Give the position of every leukocyte visible.
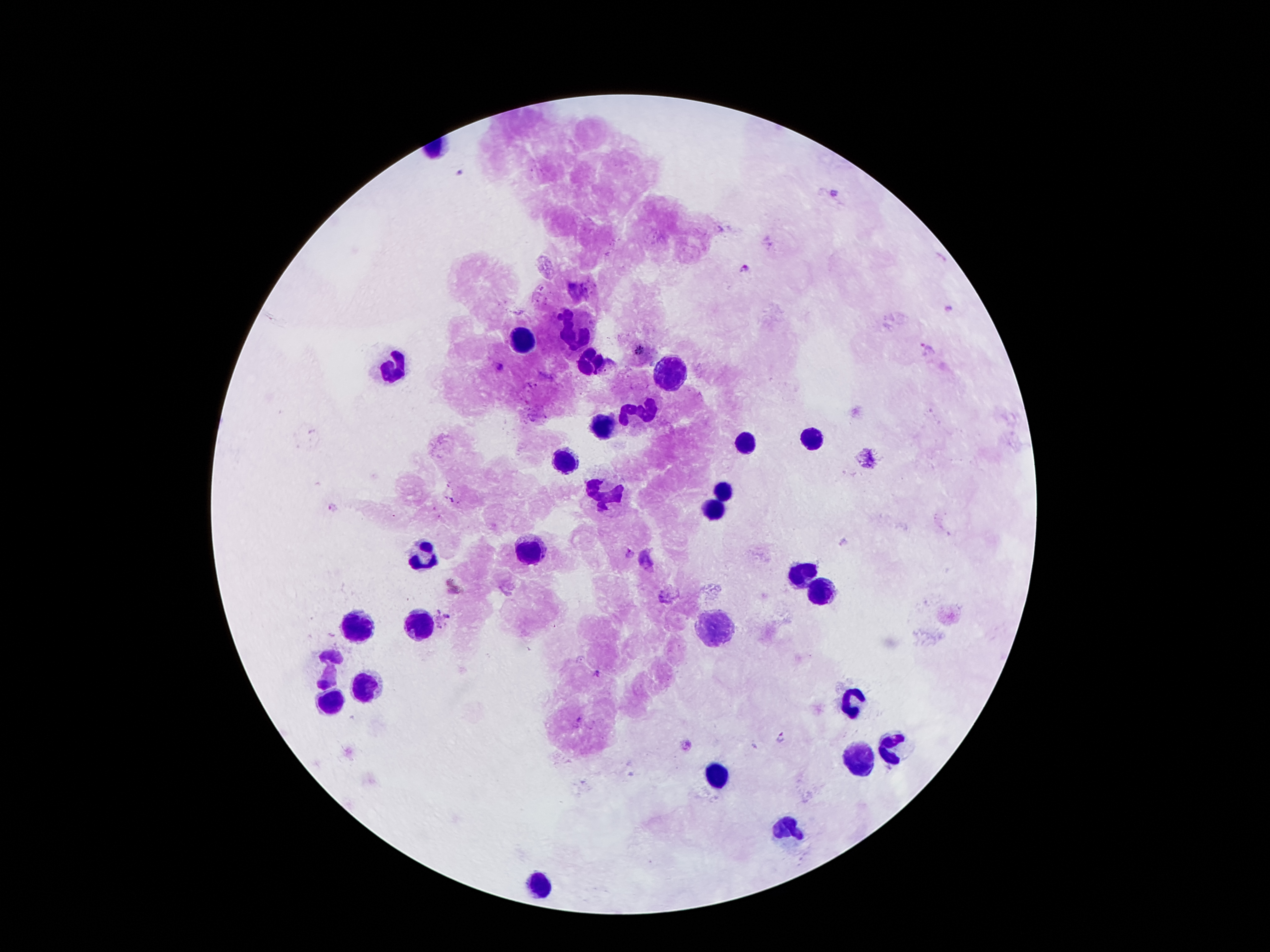
Approximate centers as {x, y} in pixels.
Leukocytes: {576, 329}, {523, 342}, {590, 364}, {393, 368}, {669, 373}, {643, 408}, {605, 426}, {813, 439}, {744, 446}, {565, 459}, {727, 488}, {605, 499}, {711, 508}, {530, 552}, {424, 556}, {798, 574}, {818, 592}, {360, 627}, {419, 627}, {720, 627}, {329, 667}, {364, 684}, {333, 700}, {851, 702}, {888, 746}, {860, 757}, {716, 773}, {784, 830}, {541, 883}.

field_of_view: one from this slide
preparation: thick peripheral-blood smear
capture: smartphone through the microscope eyepiece
patient_malaria_status: infected with Plasmodium falciparum
malaria_parasite_locations: 'approximate centers as {x, y} in pixels: {461, 173}, {834, 193}, {745, 269}, {950, 310}, {928, 350}, {498, 367}, {628, 553}, {648, 560}, {448, 616}, {597, 672}, {780, 736}'
stain: Giemsa
image_size: 1270×952 pixels
magnification: 100x